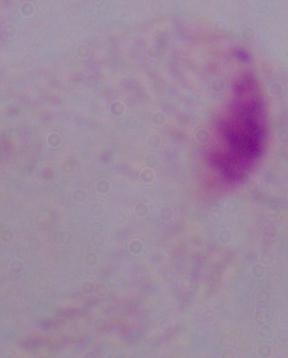
Summary:
  - Identification: trichomonad
  - Magnification: 1000x
  - Modality: photomicrograph